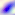

Summary:
  - Modality: micrograph
  - Magnification: 400x
  - Identification: Toxoplasma gondii